Assess the morphology of the erythrocytes.
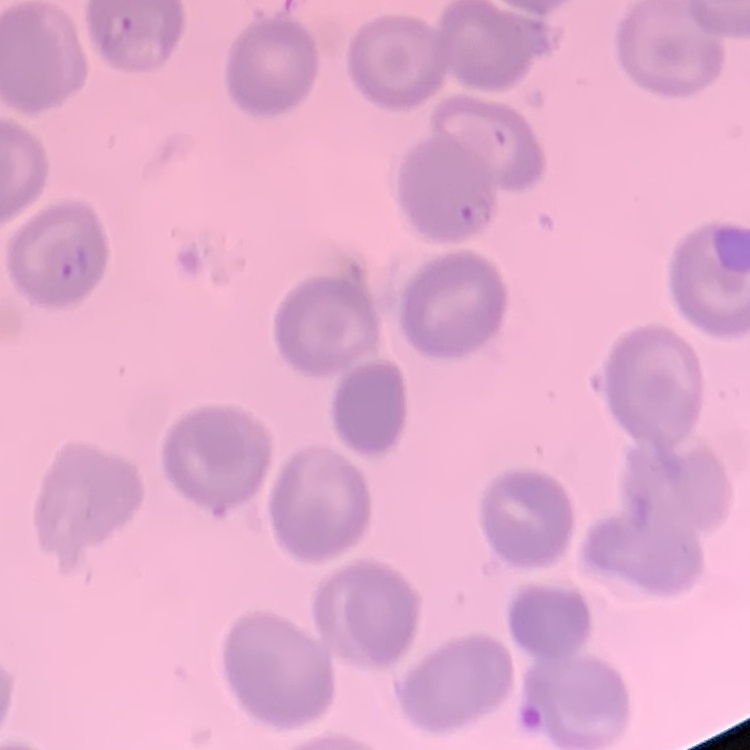

They show no rouleaux formation.

One tile cut from a larger photomicrograph. Field's or Giemsa stain. Thin peripheral smear.